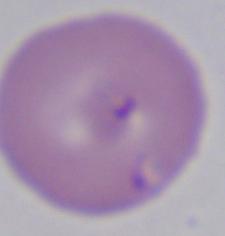

Summary:
  - Identification: Babesia
  - Modality: photomicrograph
  - Magnification: 1000x